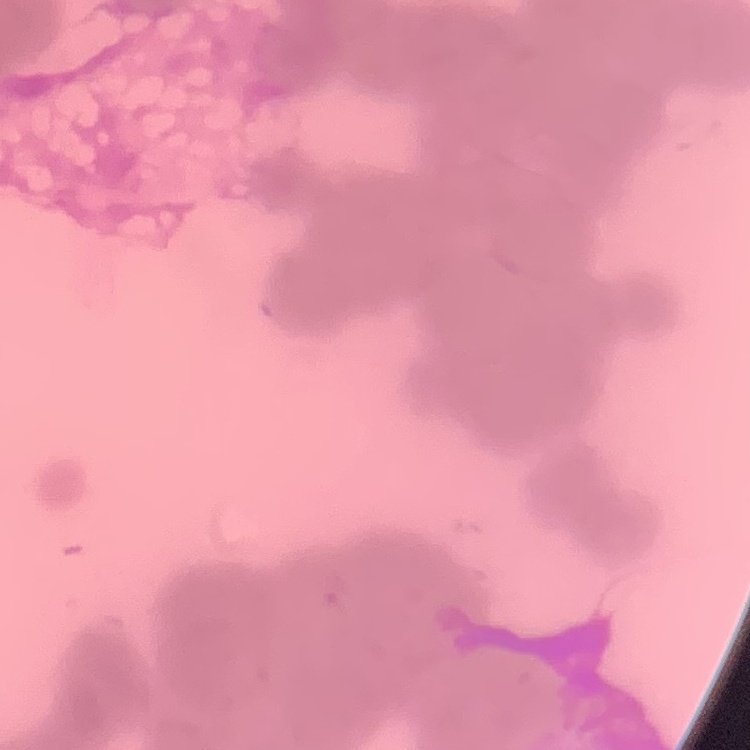

Summary:
  - Red blood cell morphology: rouleaux formation
  - Image type: one tile cut from a larger photomicrograph
  - Stain: Field's or Giemsa
  - Preparation: thin blood smear